Give the extent of all Plasmodium malariae-infected red blood cells.
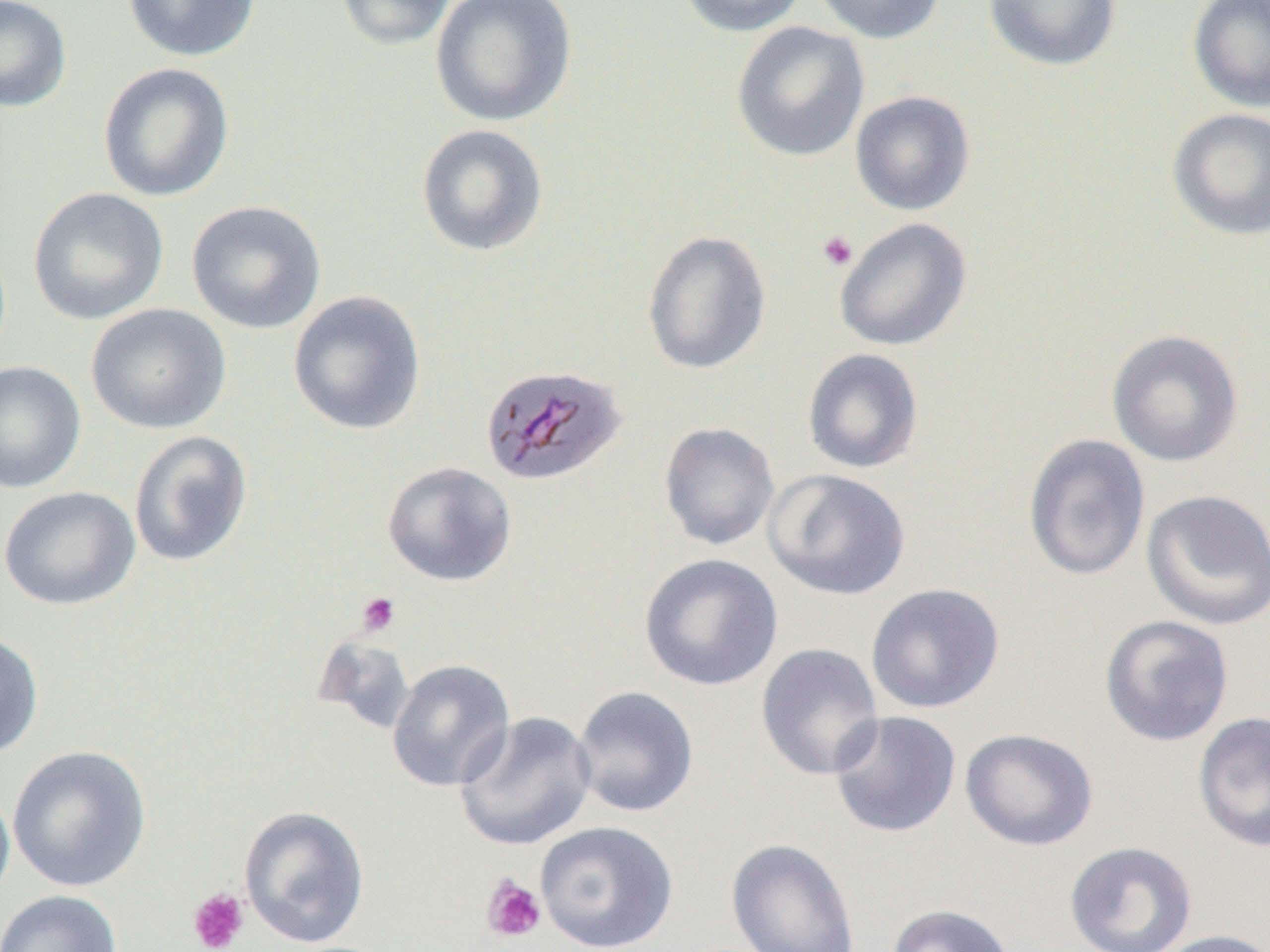
Approximate bounding boxes as [x1, y1, x2, y2] in pixels.
Plasmodium malariae-infected red blood cells: [479, 363, 627, 486].

Platelet locations: [817, 231, 858, 271], [356, 591, 401, 636], [480, 874, 546, 944], [186, 887, 249, 952]. Uninfected red blood cell locations: [0, 0, 72, 112], [122, 0, 260, 62], [335, 0, 459, 51], [430, 0, 578, 127], [675, 0, 810, 37], [811, 0, 946, 43], [983, 0, 1121, 72], [1188, 0, 1270, 112], [731, 22, 870, 162], [97, 62, 234, 202], [850, 91, 975, 216], [1166, 107, 1270, 241], [416, 124, 549, 257], [27, 187, 169, 326], [185, 200, 327, 333], [834, 217, 972, 352], [642, 229, 772, 375], [288, 290, 426, 435], [86, 303, 231, 434], [1106, 329, 1244, 468], [801, 348, 925, 474], [0, 360, 86, 494], [658, 422, 780, 550], [128, 430, 253, 567], [1023, 433, 1151, 582], [381, 461, 517, 587], [763, 468, 912, 601], [0, 486, 140, 611], [1140, 489, 1270, 631], [638, 553, 784, 691], [865, 582, 1005, 714], [1099, 615, 1234, 747], [0, 628, 44, 759], [755, 642, 885, 781], [386, 659, 516, 792], [570, 685, 699, 818], [828, 710, 962, 839], [454, 711, 597, 851], [1192, 711, 1270, 853], [960, 727, 1099, 851], [6, 745, 151, 892], [0, 781, 15, 909], [238, 805, 370, 947], [535, 820, 678, 952], [726, 838, 861, 952], [1064, 841, 1198, 952], [0, 889, 122, 952], [886, 903, 1017, 952], [1150, 929, 1270, 952]. Slide-level diagnosis: Plasmodium malariae. Image is 1270×952 pixels. Light microscopy. 1000x magnification. Thin blood film. Single field of view.